Identify the parasite.
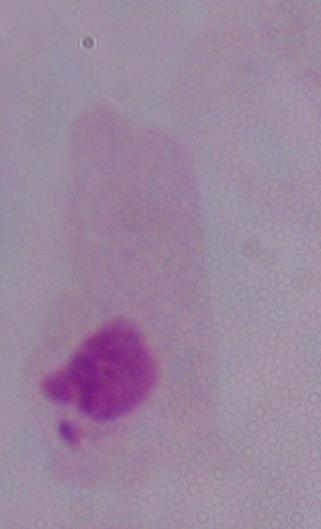
This is a trichomonad.

Summary:
  - Magnification: 1000x
  - Modality: micrograph